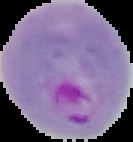

image_size: 133×142 pixels
image_type: cell region segmented out of the field of view; surrounding area masked to black
preparation: thin blood smear
malaria_status: parasitized